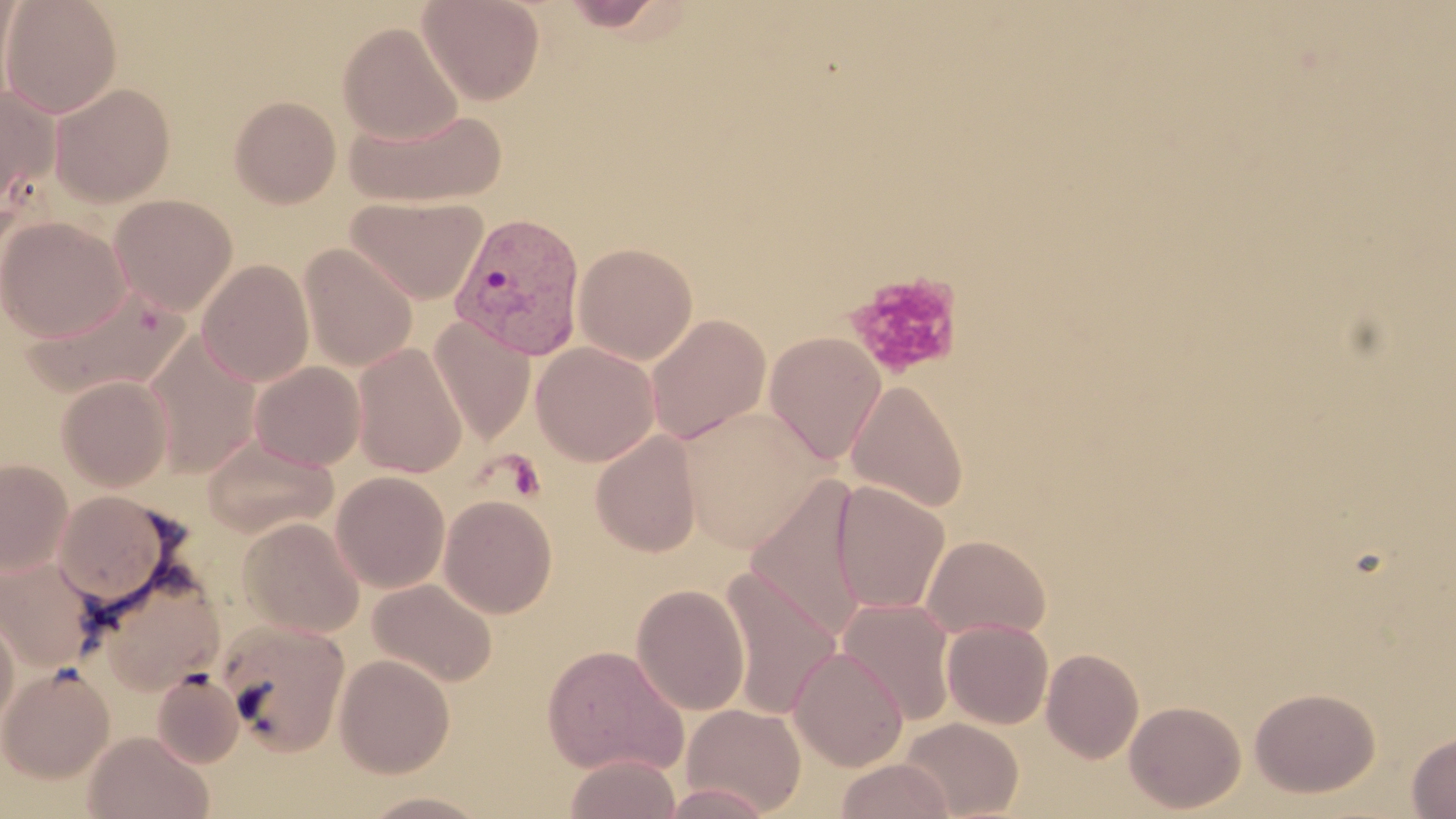

slide-level diagnosis = Plasmodium vivax
image size = 1456×819 pixels
platelet locations = approximate bounding boxes as (x1, y1, x2, y2) in pixels: (844, 271, 964, 381), (501, 451, 546, 502)
Plasmodium vivax-infected red blood cell locations = approximate bounding boxes as (x1, y1, x2, y2) in pixels: (449, 212, 587, 360)
preparation = thin blood smear
modality = optical microscopy
magnification = 1000x
uninfected red blood cell locations = approximate bounding boxes as (x1, y1, x2, y2) in pixels: (0, 0, 122, 118), (0, 0, 23, 108), (418, 0, 545, 105), (555, 0, 677, 32), (338, 22, 463, 145), (50, 83, 176, 207), (0, 84, 60, 214), (229, 96, 341, 208), (344, 105, 507, 207), (109, 194, 238, 315), (347, 195, 487, 304), (1, 216, 130, 341), (574, 242, 698, 364), (299, 243, 418, 371), (197, 260, 314, 387), (26, 283, 188, 398), (646, 314, 771, 444), (429, 317, 535, 445), (764, 331, 886, 465), (145, 333, 262, 479), (351, 342, 468, 479), (531, 342, 660, 466), (249, 361, 365, 470), (56, 375, 173, 492), (846, 379, 968, 514), (677, 407, 830, 552), (590, 431, 702, 557), (201, 436, 337, 538), (0, 457, 72, 575), (331, 471, 450, 592), (745, 476, 870, 642), (831, 480, 950, 615), (52, 490, 181, 608), (439, 494, 557, 618), (238, 516, 365, 638), (919, 534, 1051, 641), (1, 553, 101, 673), (88, 562, 227, 696), (717, 569, 843, 719), (367, 578, 498, 688), (631, 583, 750, 716), (837, 596, 957, 725), (0, 605, 19, 738), (216, 619, 351, 756), (942, 619, 1053, 729), (542, 644, 688, 776), (789, 646, 909, 771), (1042, 647, 1144, 763), (334, 653, 455, 778), (1, 663, 115, 783), (152, 670, 245, 768), (1249, 686, 1381, 797), (1124, 700, 1246, 813), (680, 702, 807, 816), (898, 717, 1024, 819), (82, 730, 213, 819), (1407, 730, 1456, 818), (563, 754, 682, 819), (834, 758, 955, 819), (356, 790, 495, 818)
field of view = single
stain = May-Grünwald-Giemsa